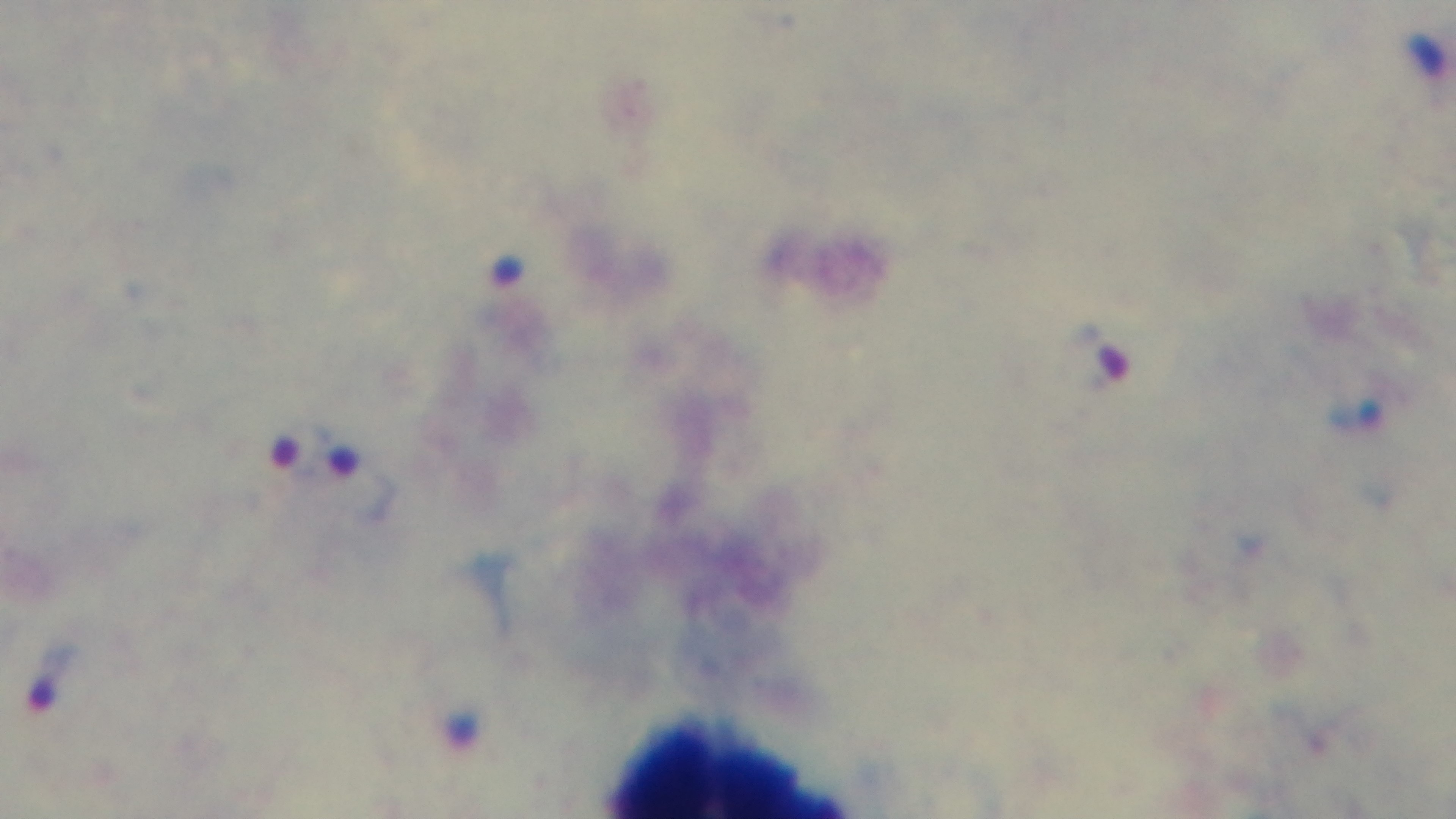
Summary:
  - Stain: Giemsa
  - Modality: light microscopy
  - Objective: 100x oil immersion
  - Preparation: thick blood film
  - Malaria status: infected
  - Field of view: one from the slide
  - Capture: mounted 4K digital camera